Classify this cell by malaria status.
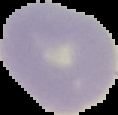
It is uninfected.

image type = segmented cell region with the area outside set to black
preparation = thin blood film
image size = 118×115 pixels